Assess this cell for malaria.
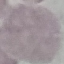

Uninfected.

Automatically extracted cell patch, resized to 64 × 64 pixels. Giemsa-stained preparation. Thin smear of blood. Acquired by smartphone through the microscope eyepiece.